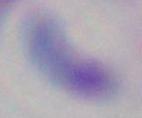

Summary:
  - Modality: photomicrograph
  - Identification: Toxoplasma gondii
  - Magnification: 1000x